Give the position of every Plasmodium parasite.
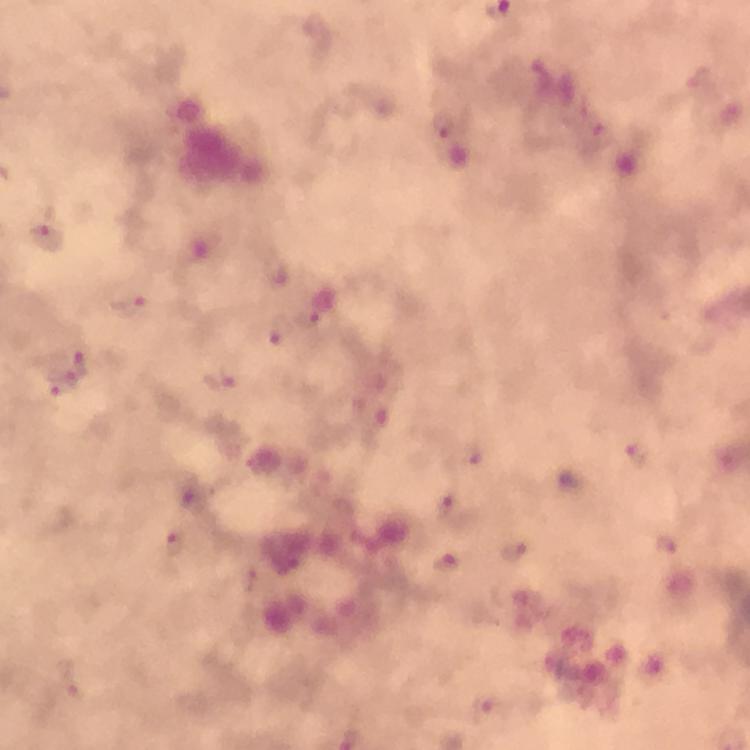
Approximate centers as (x, y) in pixels.
Plasmodium parasites: (442, 126), (47, 239), (130, 307), (281, 330), (77, 366), (222, 380), (63, 382), (636, 453), (453, 508), (174, 543), (666, 543), (514, 550), (446, 564).

context = from a diagnostic examination for malaria
magnification = 100x
capture = smartphone camera through the microscope
stain = Giemsa
preparation = thick blood film
cropped from = a single field of view
image size = 750×750 pixels
immersion oil = applied